Locate platelets.
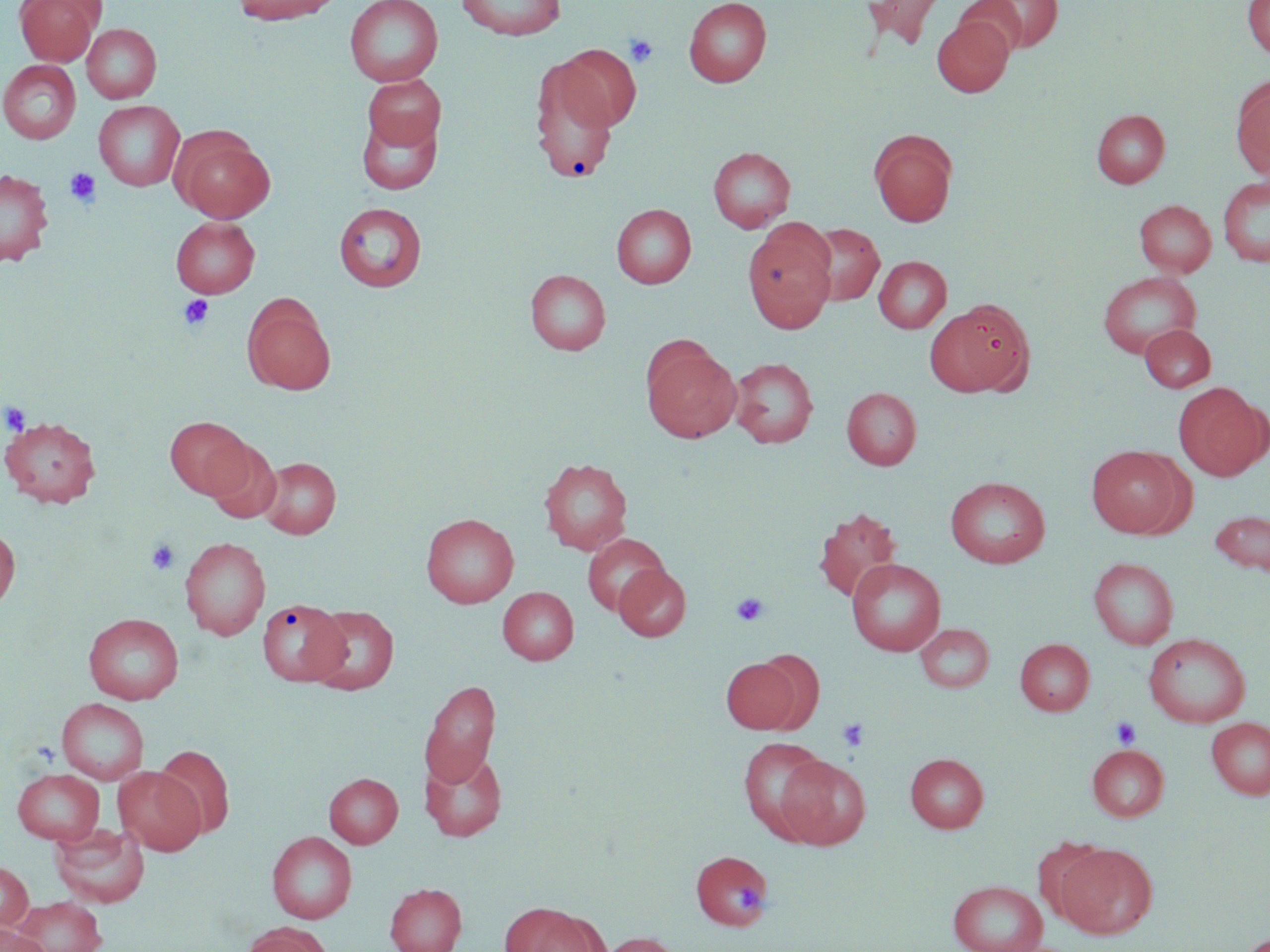
Approximate bounding boxes as (x1,y1)-(x2,y2) corner pairs in pixels.
Platelets: (624,33)-(659,68), (64,169)-(101,207), (178,295)-(214,330), (1,401)-(31,435), (146,538)-(181,575), (730,591)-(769,627), (1111,715)-(1142,748), (837,717)-(870,752), (736,884)-(764,912).

Summary:
  - Uninfected red blood cell locations: (14,0)-(103,66), (231,0)-(339,25), (344,0)-(443,87), (456,0)-(567,39), (683,0)-(771,87), (861,0)-(947,48), (968,0)-(1062,54), (1242,0)-(1270,58), (932,16)-(1014,97), (82,23)-(161,103), (555,44)-(641,130), (531,50)-(626,184), (0,60)-(81,144), (362,74)-(445,152), (1231,77)-(1270,180), (94,100)-(184,191), (1091,109)-(1170,188), (357,110)-(443,195), (870,129)-(958,227), (173,132)-(275,223), (707,146)-(796,232), (0,168)-(53,266), (1217,176)-(1270,267), (1135,200)-(1216,276), (333,202)-(427,292), (611,203)-(696,288), (170,217)-(259,298), (742,222)-(838,333), (801,223)-(885,306), (873,256)-(951,333), (525,269)-(610,355), (1097,271)-(1202,358), (242,295)-(336,395), (927,299)-(1036,397), (1140,324)-(1216,392), (642,340)-(741,442), (729,357)-(819,447), (1174,383)-(1269,480), (842,387)-(921,469), (1,416)-(101,507), (164,416)-(252,499), (204,438)-(282,524), (1086,445)-(1190,538), (257,455)-(342,539), (538,457)-(633,555), (946,477)-(1050,568), (813,507)-(903,603), (1209,510)-(1270,578), (421,513)-(519,608), (0,525)-(20,613), (583,534)-(669,616), (179,536)-(271,640), (1088,557)-(1178,649), (847,558)-(946,655), (614,563)-(691,642), (498,586)-(578,665), (257,599)-(349,686), (305,605)-(399,695), (83,612)-(184,704), (915,623)-(995,692), (1144,633)-(1250,727), (1014,638)-(1094,715), (720,657)-(803,734), (419,679)-(500,788), (56,697)-(150,785), (1207,717)-(1270,799), (739,737)-(832,841), (1087,743)-(1169,821), (154,745)-(235,839), (419,749)-(507,842), (905,753)-(988,832), (775,754)-(871,849), (113,766)-(205,855), (12,768)-(105,844), (324,773)-(403,848), (49,822)-(149,908), (267,831)-(357,923), (1053,842)-(1157,940), (692,849)-(773,931), (0,861)-(33,931), (947,880)-(1048,952), (385,883)-(466,952), (11,896)-(107,952), (499,903)-(604,952), (240,922)-(331,952), (0,925)-(49,952), (597,932)-(683,952)
  - Slide-level diagnosis: no evidence of blood parasites
  - Field of view: single
  - Preparation: thin blood film
  - Modality: light microscopy
  - Image size: 1270×952 pixels
  - Magnification: 1000x
  - Stain: May-Grünwald-Giemsa